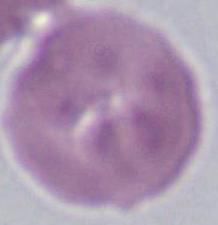

1000x magnification. A red blood cell is seen. Micrograph.